Assess this cell for malaria.
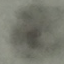

Uninfected.

stain = Giemsa
image type = automatically extracted cell patch, resized to 64 × 64 pixels
preparation = thin blood film
capture = smartphone camera at the microscope eyepiece